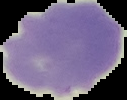
Malaria status: uninfected. From a thin blood smear. Segmented cell region on a black background. Image is 127×100 pixels.